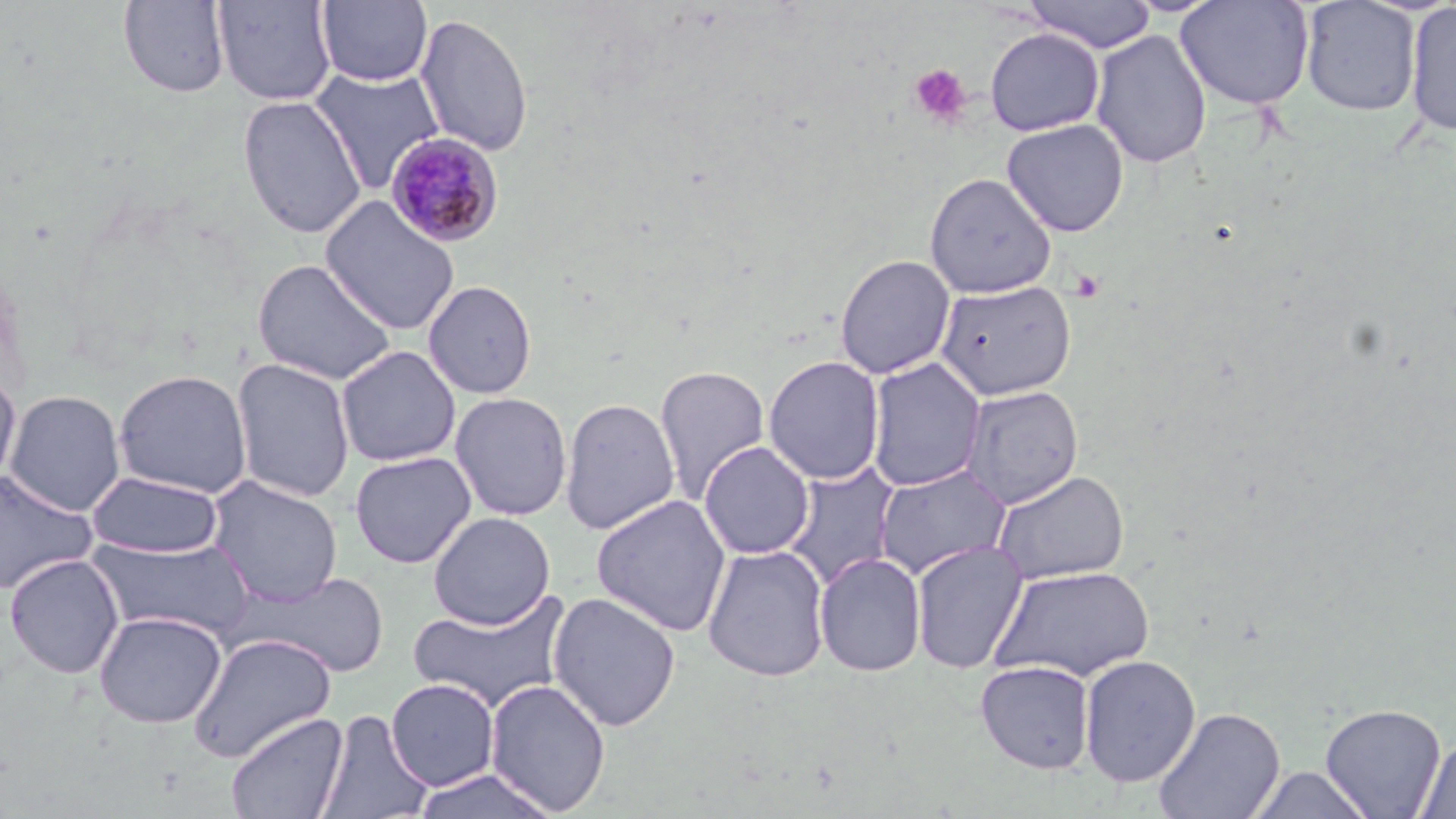

Approximate bounding boxes as named x1/y1/x2/y2 corners in pixels. Uninfected red blood cell locations: (x1=212, y1=0, x2=337, y2=106), (x1=1022, y1=0, x2=1157, y2=53), (x1=1300, y1=0, x2=1421, y2=117), (x1=118, y1=1, x2=231, y2=98), (x1=316, y1=1, x2=433, y2=86), (x1=1176, y1=1, x2=1315, y2=111), (x1=1404, y1=2, x2=1456, y2=137), (x1=413, y1=12, x2=534, y2=157), (x1=985, y1=27, x2=1105, y2=136), (x1=1090, y1=29, x2=1212, y2=169), (x1=308, y1=66, x2=446, y2=195), (x1=237, y1=95, x2=367, y2=240), (x1=1001, y1=118, x2=1129, y2=237), (x1=923, y1=172, x2=1057, y2=298), (x1=319, y1=196, x2=460, y2=335), (x1=834, y1=254, x2=956, y2=379), (x1=251, y1=258, x2=398, y2=386), (x1=422, y1=279, x2=538, y2=399), (x1=934, y1=279, x2=1077, y2=400), (x1=336, y1=345, x2=461, y2=467), (x1=763, y1=355, x2=886, y2=485), (x1=866, y1=357, x2=986, y2=492), (x1=231, y1=358, x2=355, y2=503), (x1=653, y1=364, x2=770, y2=504), (x1=112, y1=369, x2=253, y2=498), (x1=0, y1=373, x2=21, y2=491), (x1=961, y1=384, x2=1084, y2=509), (x1=4, y1=389, x2=127, y2=517), (x1=450, y1=391, x2=573, y2=521), (x1=559, y1=396, x2=680, y2=534), (x1=699, y1=440, x2=815, y2=560), (x1=349, y1=450, x2=477, y2=569), (x1=782, y1=461, x2=901, y2=589), (x1=873, y1=464, x2=1011, y2=580), (x1=0, y1=467, x2=98, y2=595), (x1=87, y1=469, x2=223, y2=559), (x1=991, y1=469, x2=1130, y2=585), (x1=205, y1=475, x2=344, y2=607), (x1=590, y1=494, x2=732, y2=637), (x1=428, y1=511, x2=555, y2=630), (x1=87, y1=534, x2=256, y2=641), (x1=910, y1=539, x2=1029, y2=674), (x1=702, y1=544, x2=831, y2=682), (x1=814, y1=552, x2=927, y2=677), (x1=4, y1=553, x2=125, y2=679), (x1=989, y1=565, x2=1154, y2=682), (x1=248, y1=570, x2=391, y2=677), (x1=406, y1=588, x2=573, y2=714), (x1=547, y1=591, x2=681, y2=732), (x1=93, y1=610, x2=227, y2=728), (x1=187, y1=633, x2=338, y2=763), (x1=1079, y1=654, x2=1201, y2=787), (x1=975, y1=660, x2=1095, y2=774), (x1=385, y1=678, x2=499, y2=791), (x1=485, y1=679, x2=612, y2=815), (x1=1320, y1=702, x2=1447, y2=818), (x1=1152, y1=706, x2=1286, y2=819), (x1=317, y1=709, x2=433, y2=819), (x1=225, y1=710, x2=349, y2=819), (x1=1414, y1=737, x2=1456, y2=819), (x1=1247, y1=765, x2=1374, y2=819), (x1=409, y1=769, x2=560, y2=819). Platelet locations: (x1=909, y1=64, x2=972, y2=127). Plasmodium malariae-infected red blood cell locations: (x1=386, y1=131, x2=504, y2=248). Slide-level diagnosis: Plasmodium malariae. Light microscopy. May-Grünwald-Giemsa stain. One field of a larger specimen. Image is 1456×819 pixels. Thin blood smear. Captured at 1000x magnification.